Locate every blood parasite and identify its species.
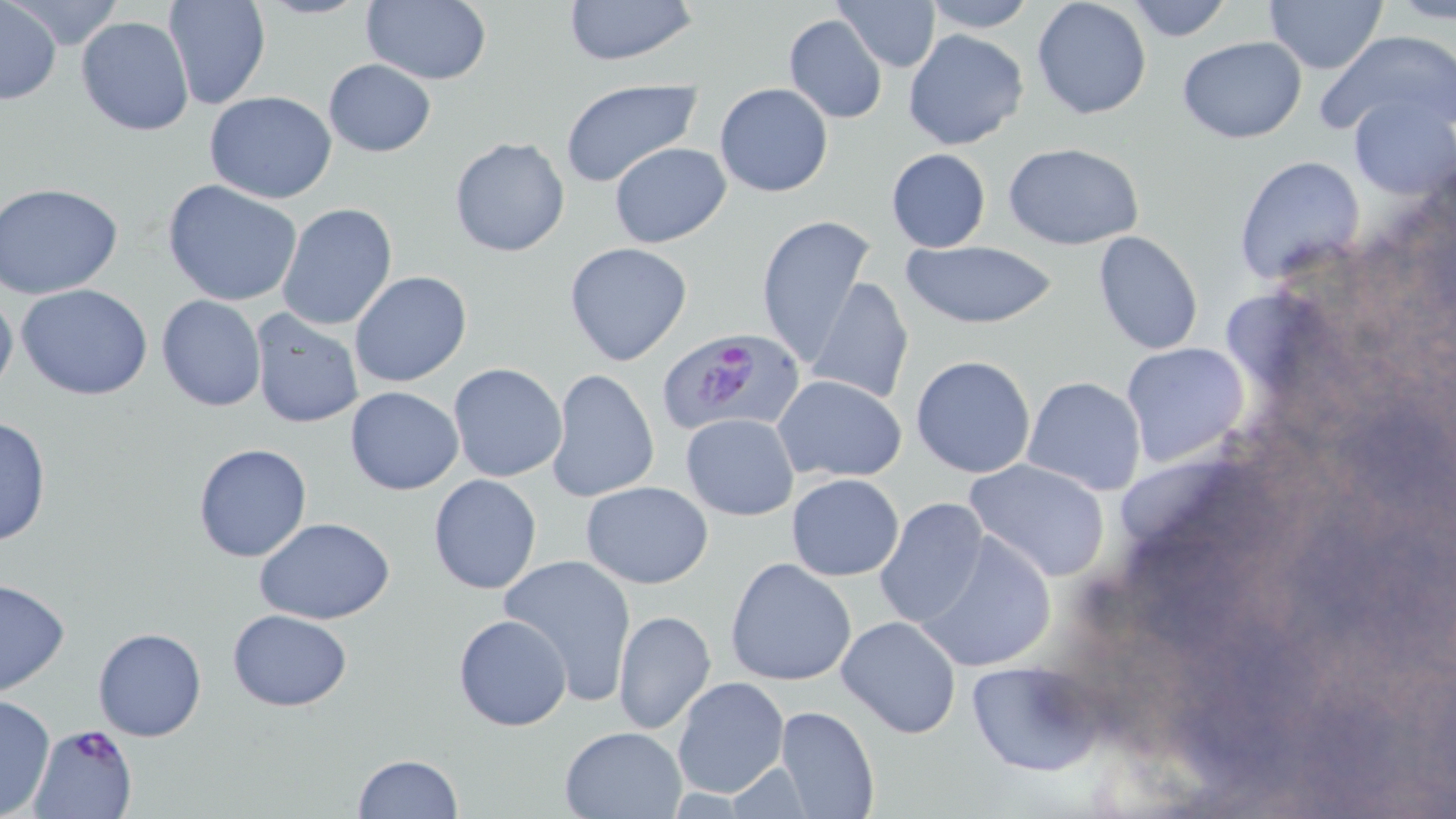
Approximate bounding boxes as [x1, y1, x2, y2] in pixels.
Plasmodium falciparum-infected red blood cells: [657, 328, 808, 439], [28, 724, 137, 818].
No Plasmodium ovale, Plasmodium malariae, Plasmodium vivax, Babesia divergens, or Trypanosoma brucei observed.

Summary:
  - Uninfected red blood cell locations: [163, 0, 270, 111], [360, 0, 493, 85], [558, 0, 700, 68], [834, 0, 941, 72], [1030, 0, 1153, 121], [1123, 0, 1233, 42], [1263, 0, 1386, 73], [1387, 0, 1456, 25], [1, 1, 61, 105], [921, 1, 1037, 32], [782, 14, 889, 124], [75, 15, 194, 136], [904, 29, 1029, 151], [1319, 31, 1455, 138], [1177, 35, 1307, 143], [322, 58, 436, 157], [556, 78, 703, 190], [714, 83, 834, 197], [205, 92, 337, 204], [1349, 97, 1455, 201], [448, 136, 571, 257], [609, 141, 732, 247], [1004, 142, 1145, 251], [885, 148, 992, 252], [1232, 155, 1364, 287], [162, 180, 303, 307], [0, 181, 123, 299], [277, 202, 399, 331], [753, 213, 875, 371], [1092, 230, 1206, 356], [901, 239, 1060, 330], [564, 242, 693, 367], [349, 271, 472, 388], [808, 277, 915, 408], [0, 280, 18, 405], [17, 283, 153, 400], [156, 294, 267, 411], [248, 308, 364, 429], [1120, 342, 1250, 468], [911, 355, 1036, 478], [447, 363, 567, 483], [545, 369, 661, 505], [773, 375, 907, 483], [1022, 375, 1146, 496], [345, 385, 464, 495], [679, 413, 800, 521], [0, 414, 52, 548], [192, 443, 313, 563], [965, 458, 1111, 583], [786, 473, 905, 582], [428, 475, 542, 593], [580, 481, 715, 588], [872, 498, 993, 629], [254, 517, 396, 624], [915, 526, 1058, 674], [498, 552, 639, 705], [725, 558, 856, 686], [0, 578, 71, 697], [226, 609, 352, 711], [612, 610, 716, 735], [452, 614, 572, 731], [836, 614, 962, 740], [93, 627, 206, 741], [964, 660, 1103, 778], [671, 676, 790, 799], [0, 695, 56, 818], [774, 704, 879, 818], [559, 725, 689, 818], [353, 755, 463, 818]
  - Slide-level diagnosis: Plasmodium falciparum
  - Image size: 1456×819 pixels
  - Magnification: 1000x
  - Modality: light microscopy
  - Preparation: thin blood film
  - Field of view: single
  - Stain: May-Grünwald-Giemsa